Locate every blood parasite and identify its species.
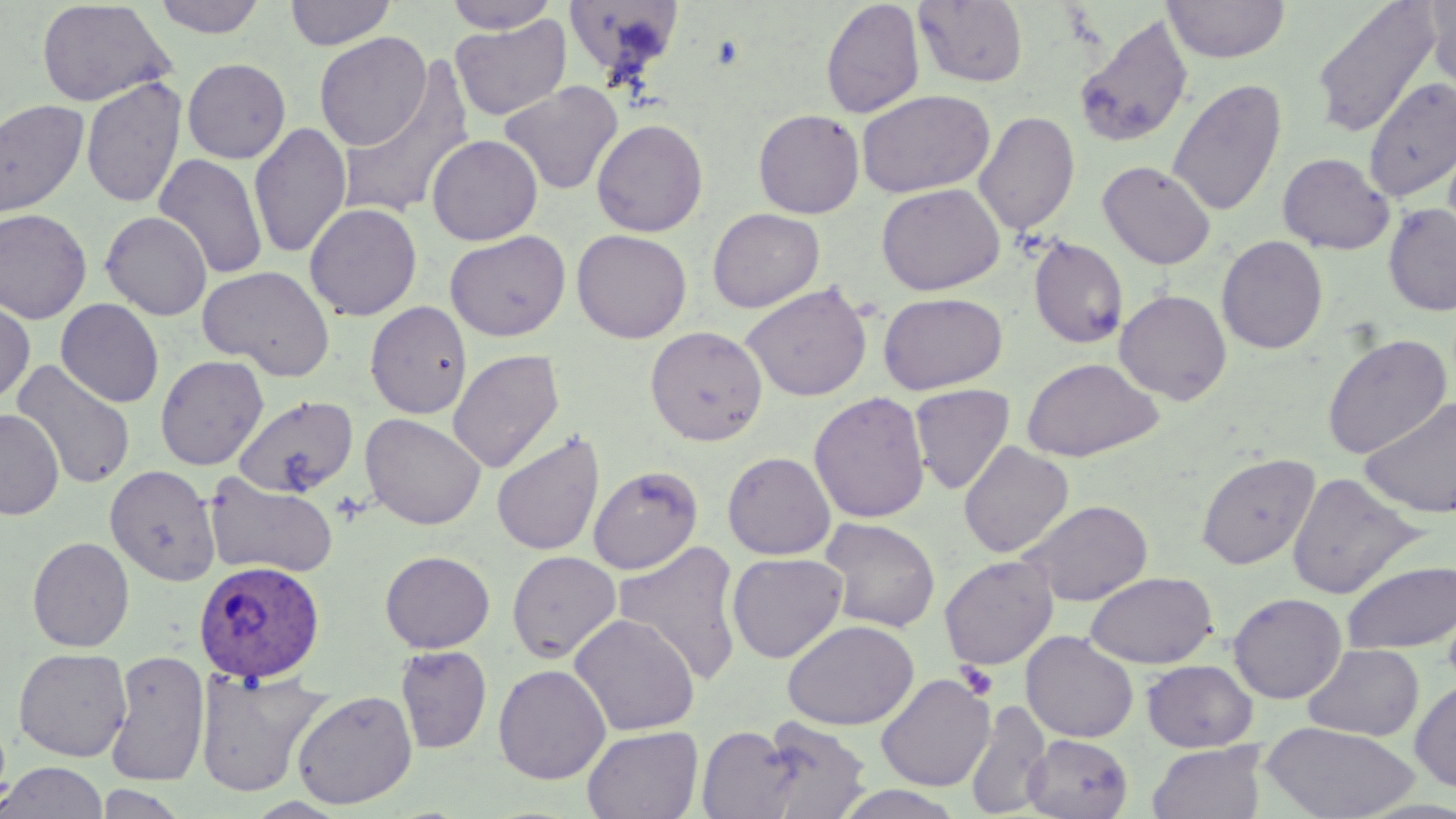
Approximate bounding boxes as named x1/y1/x2/y2 corners in pixels.
Plasmodium ovale-infected red blood cells: (x1=193, y1=559, x2=326, y2=685).
No Plasmodium falciparum, Plasmodium malariae, Plasmodium vivax, Babesia divergens, or Trypanosoma brucei observed.

{
  "slide_level_diagnosis": "Plasmodium ovale",
  "platelet_locations": "approximate bounding boxes as named x1/y1/x2/y2 corners in pixels: (x1=956, y1=662, x2=999, y2=700)",
  "preparation": "thin blood smear",
  "uninfected_red_blood_cell_locations": "approximate bounding boxes as named x1/y1/x2/y2 corners in pixels: (x1=151, y1=0, x2=268, y2=38), (x1=285, y1=0, x2=396, y2=50), (x1=442, y1=0, x2=561, y2=33), (x1=1162, y1=0, x2=1291, y2=63), (x1=1311, y1=0, x2=1443, y2=140), (x1=1425, y1=0, x2=1456, y2=96), (x1=36, y1=1, x2=174, y2=107), (x1=820, y1=1, x2=925, y2=119), (x1=912, y1=1, x2=1028, y2=88), (x1=562, y1=3, x2=687, y2=85), (x1=1074, y1=13, x2=1194, y2=149), (x1=450, y1=15, x2=571, y2=121), (x1=314, y1=32, x2=432, y2=151), (x1=182, y1=58, x2=291, y2=163), (x1=335, y1=61, x2=477, y2=221), (x1=81, y1=76, x2=186, y2=210), (x1=1363, y1=77, x2=1456, y2=202), (x1=1167, y1=79, x2=1287, y2=218), (x1=499, y1=81, x2=623, y2=196), (x1=856, y1=89, x2=996, y2=198), (x1=0, y1=99, x2=90, y2=220), (x1=753, y1=109, x2=865, y2=218), (x1=974, y1=110, x2=1079, y2=236), (x1=591, y1=118, x2=709, y2=237), (x1=249, y1=121, x2=352, y2=260), (x1=426, y1=134, x2=543, y2=245), (x1=1278, y1=152, x2=1394, y2=254), (x1=154, y1=153, x2=268, y2=280), (x1=1098, y1=160, x2=1216, y2=270), (x1=876, y1=183, x2=1005, y2=295), (x1=304, y1=202, x2=422, y2=321), (x1=1383, y1=202, x2=1456, y2=317), (x1=0, y1=208, x2=92, y2=323), (x1=707, y1=208, x2=825, y2=313), (x1=100, y1=211, x2=212, y2=320), (x1=571, y1=229, x2=692, y2=343), (x1=445, y1=230, x2=570, y2=341), (x1=1029, y1=235, x2=1128, y2=348), (x1=1217, y1=235, x2=1328, y2=354), (x1=197, y1=265, x2=336, y2=380), (x1=741, y1=282, x2=873, y2=401), (x1=1115, y1=289, x2=1232, y2=405), (x1=878, y1=291, x2=1008, y2=395), (x1=0, y1=298, x2=35, y2=405), (x1=56, y1=298, x2=164, y2=407), (x1=365, y1=300, x2=472, y2=418), (x1=645, y1=325, x2=768, y2=445), (x1=1322, y1=332, x2=1451, y2=460), (x1=448, y1=349, x2=565, y2=473), (x1=155, y1=354, x2=269, y2=470), (x1=1021, y1=357, x2=1164, y2=462), (x1=13, y1=360, x2=135, y2=490), (x1=909, y1=384, x2=1015, y2=495), (x1=809, y1=391, x2=931, y2=523), (x1=234, y1=395, x2=359, y2=498), (x1=1360, y1=397, x2=1456, y2=518), (x1=0, y1=409, x2=64, y2=520), (x1=360, y1=413, x2=486, y2=530), (x1=491, y1=429, x2=605, y2=557), (x1=959, y1=441, x2=1074, y2=558), (x1=722, y1=451, x2=836, y2=561), (x1=1196, y1=452, x2=1321, y2=570), (x1=105, y1=465, x2=221, y2=586), (x1=588, y1=465, x2=703, y2=574), (x1=1286, y1=471, x2=1421, y2=601), (x1=204, y1=472, x2=339, y2=579), (x1=1020, y1=499, x2=1154, y2=606), (x1=819, y1=517, x2=940, y2=633), (x1=27, y1=536, x2=134, y2=652), (x1=613, y1=540, x2=745, y2=687), (x1=379, y1=550, x2=495, y2=653), (x1=506, y1=550, x2=621, y2=663), (x1=727, y1=552, x2=847, y2=663), (x1=939, y1=554, x2=1059, y2=671), (x1=1341, y1=559, x2=1456, y2=655), (x1=1084, y1=571, x2=1218, y2=669), (x1=1228, y1=592, x2=1347, y2=704), (x1=569, y1=614, x2=700, y2=736), (x1=783, y1=619, x2=919, y2=730), (x1=1021, y1=631, x2=1139, y2=743), (x1=1301, y1=643, x2=1424, y2=741), (x1=395, y1=645, x2=493, y2=754), (x1=13, y1=647, x2=132, y2=762), (x1=104, y1=650, x2=210, y2=787), (x1=1142, y1=659, x2=1258, y2=752), (x1=493, y1=663, x2=611, y2=784), (x1=194, y1=668, x2=330, y2=797), (x1=876, y1=672, x2=995, y2=791), (x1=1410, y1=678, x2=1456, y2=793), (x1=292, y1=688, x2=417, y2=809), (x1=965, y1=699, x2=1052, y2=817), (x1=756, y1=717, x2=872, y2=819), (x1=1260, y1=721, x2=1421, y2=819), (x1=696, y1=724, x2=803, y2=818), (x1=581, y1=725, x2=703, y2=819), (x1=1024, y1=734, x2=1133, y2=818), (x1=1147, y1=742, x2=1266, y2=819), (x1=0, y1=761, x2=107, y2=819), (x1=95, y1=784, x2=190, y2=819), (x1=832, y1=785, x2=969, y2=819)",
  "field_of_view": "one of a larger specimen",
  "magnification": "1000x",
  "modality": "optical microscopy",
  "image_size": "1456×819 pixels",
  "stain": "May-Grünwald-Giemsa"
}